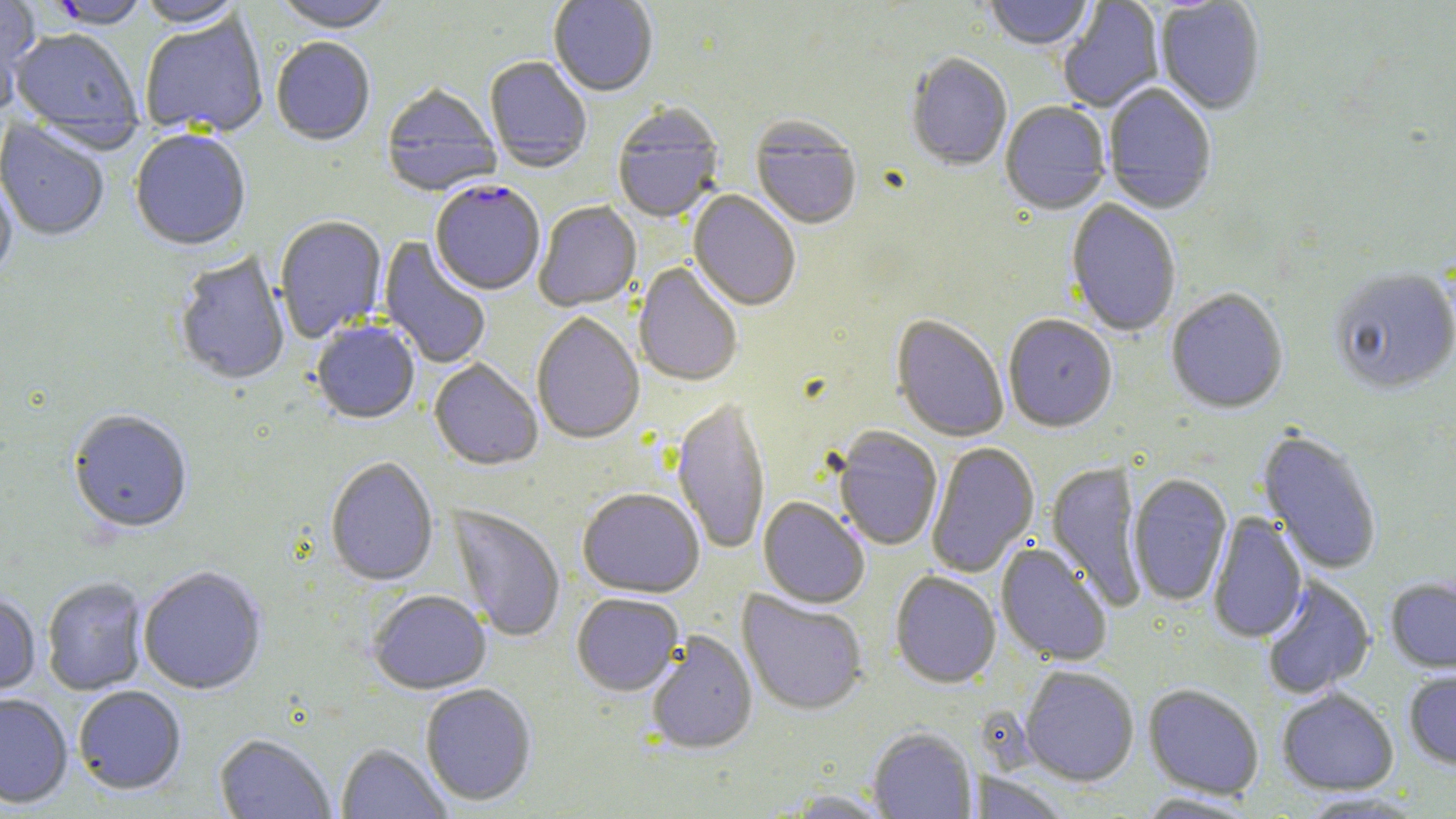
Summary:
  - Coordinate format: approximate bounding boxes as (x1,y1)-(x2,y2) corner pairs in pixels
  - Plasmodium falciparum-infected red blood cell locations: (44,1)-(150,31), (430,182)-(545,297)
  - Uninfected red blood cell locations: (0,0)-(40,113), (271,0)-(396,36), (548,0)-(658,98), (983,0)-(1094,53), (1058,0)-(1165,113), (134,1)-(247,30), (1155,1)-(1266,116), (139,15)-(269,139), (10,29)-(143,149), (271,40)-(375,147), (905,55)-(1012,172), (484,57)-(592,173), (1103,84)-(1216,216), (381,85)-(501,198), (999,103)-(1111,217), (612,106)-(724,225), (0,119)-(109,243), (750,119)-(862,232), (130,131)-(251,253), (0,174)-(17,285), (687,191)-(800,312), (1065,200)-(1181,338), (534,201)-(642,313), (275,216)-(387,343), (378,236)-(492,370), (174,252)-(291,387), (633,264)-(742,388), (1329,271)-(1456,397), (1166,290)-(1288,415), (531,313)-(645,446), (891,315)-(1009,443), (1003,316)-(1117,434), (311,322)-(420,425), (429,360)-(543,471), (672,398)-(770,556), (68,411)-(192,536), (832,427)-(942,552), (1256,428)-(1383,575), (926,442)-(1040,578), (324,458)-(439,587), (1046,461)-(1148,611), (1128,474)-(1232,607), (577,489)-(705,599), (758,497)-(870,609), (447,505)-(565,644), (1207,513)-(1308,644), (996,542)-(1113,667), (138,567)-(267,696), (890,571)-(1001,689), (1260,575)-(1376,699), (41,577)-(148,695), (1386,577)-(1456,674), (737,590)-(868,717), (368,591)-(492,695), (0,594)-(41,697), (572,594)-(684,697), (645,631)-(758,756), (1020,666)-(1139,786), (1403,668)-(1456,770), (420,684)-(537,806), (1143,684)-(1264,799), (73,686)-(187,796), (1276,688)-(1399,796), (0,694)-(73,809), (867,728)-(978,819), (215,734)-(336,818), (337,744)-(451,819), (970,771)-(1070,819), (782,789)-(898,818), (1296,792)-(1429,818), (1134,793)-(1260,818)
  - Slide-level diagnosis: Plasmodium falciparum
  - Image size: 1456×819 pixels
  - Magnification: 1000x
  - Field of view: single
  - Preparation: thin blood smear
  - Stain: May-Grünwald-Giemsa
  - Modality: optical microscopy